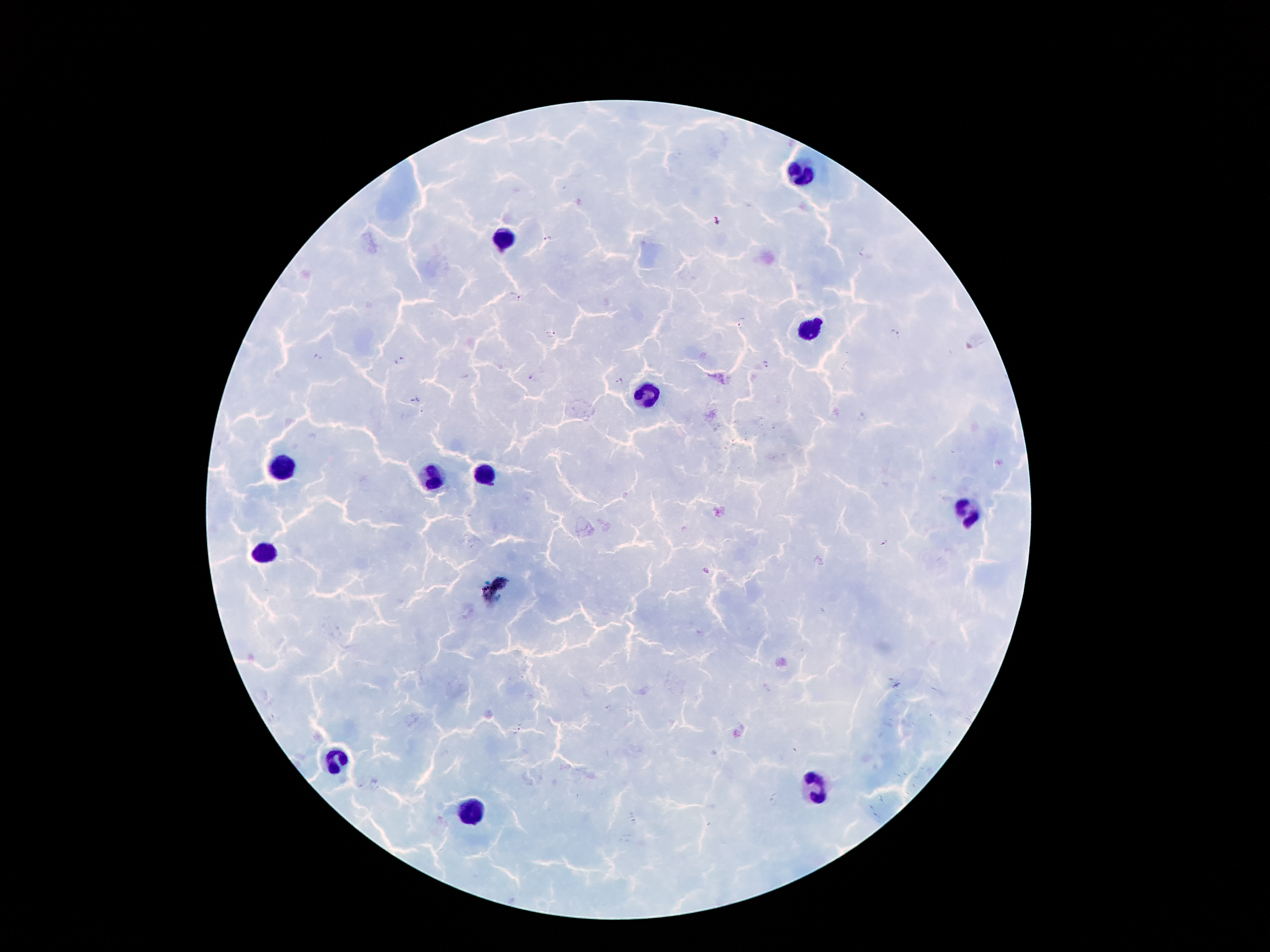

coordinate format = approximate centers as (x, y) in pixels
malaria parasite locations = (717, 222), (546, 238), (517, 294), (742, 323), (552, 334), (895, 334), (317, 358), (399, 361), (766, 363), (530, 379), (619, 382), (414, 402), (862, 418), (885, 543), (609, 707), (518, 732)
leukocyte locations = (800, 174), (502, 239), (811, 328), (646, 396), (285, 467), (486, 473), (434, 480), (966, 516), (264, 553), (337, 757), (813, 791), (473, 812)
preparation = thick blood smear
stain = Giemsa
image size = 1270×952 pixels
patient malaria status = positive for Plasmodium falciparum
magnification = 100x
capture = smartphone camera through the microscope eyepiece
field of view = one from this slide